Name the parasite shown.
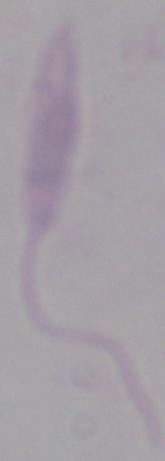
This is Leishmania.

Summary:
  - Magnification: 1000x
  - Modality: photomicrograph